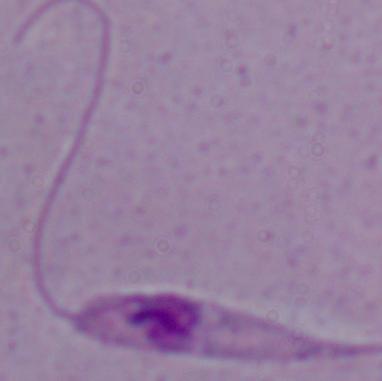

magnification = 1000x
identification = Leishmania
modality = micrograph